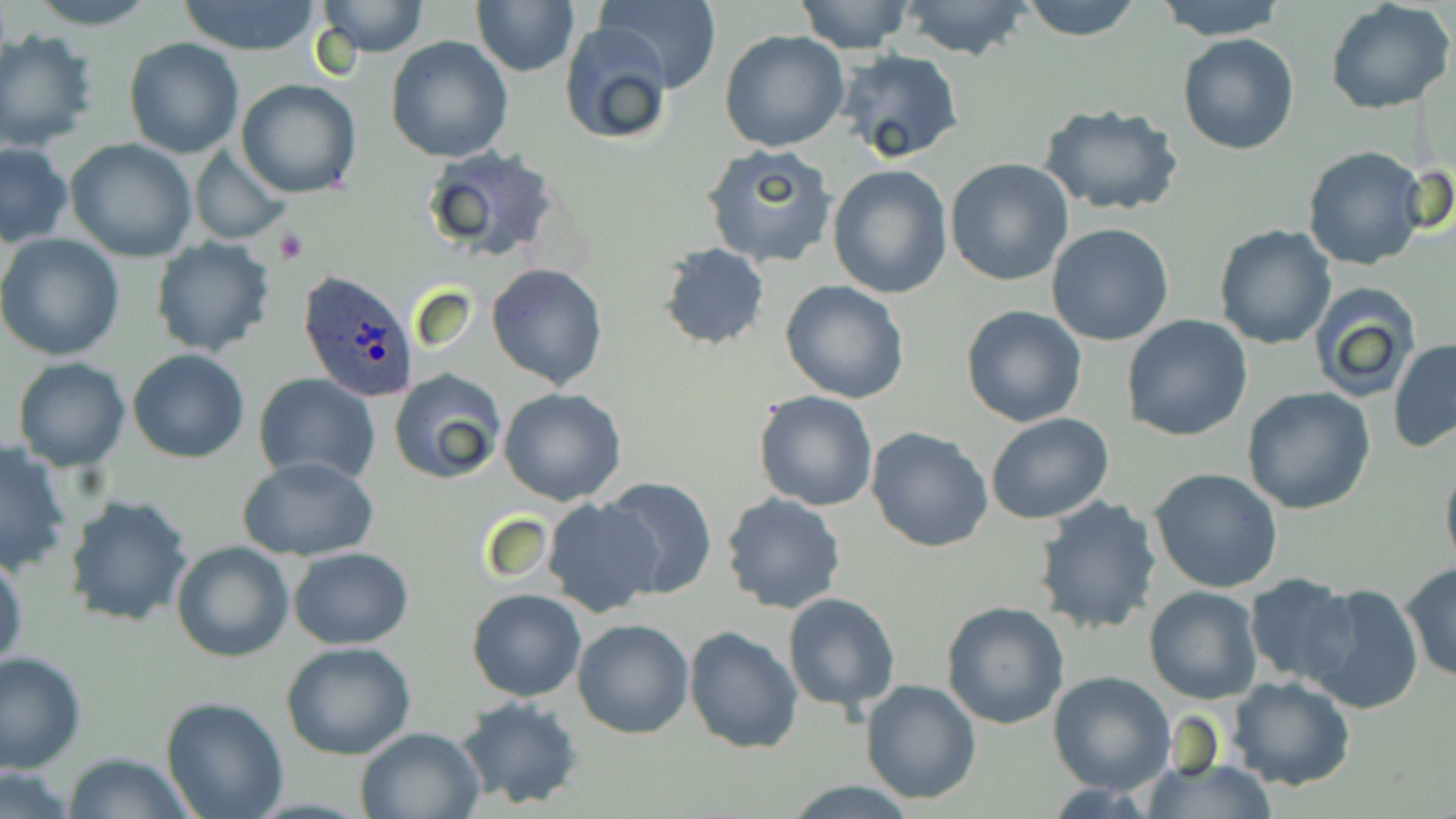

Approximate bounding boxes as [x1, y1, x2, y2] in pixels. Uninfected red blood cell locations: [21, 0, 161, 29], [173, 0, 324, 55], [315, 0, 431, 57], [793, 0, 915, 54], [898, 0, 1034, 62], [1016, 0, 1144, 42], [1152, 0, 1289, 41], [1324, 0, 1454, 115], [472, 1, 579, 76], [596, 1, 722, 93], [556, 23, 675, 147], [1, 28, 101, 152], [720, 29, 850, 152], [1176, 33, 1300, 155], [124, 37, 244, 159], [386, 37, 513, 161], [836, 50, 966, 168], [235, 79, 362, 199], [1037, 103, 1183, 216], [65, 139, 199, 261], [0, 143, 73, 248], [702, 143, 839, 269], [1302, 143, 1431, 271], [422, 145, 564, 259], [188, 146, 290, 244], [944, 157, 1075, 286], [827, 165, 953, 299], [1047, 224, 1176, 347], [1214, 224, 1337, 350], [0, 235, 125, 361], [149, 236, 275, 357], [657, 243, 770, 351], [488, 262, 607, 390], [780, 280, 910, 404], [1308, 282, 1423, 401], [960, 304, 1088, 427], [1121, 314, 1252, 442], [1389, 340, 1456, 452], [128, 350, 250, 462], [13, 356, 131, 471], [388, 370, 507, 484], [254, 374, 380, 484], [499, 387, 626, 505], [1242, 387, 1376, 514], [753, 391, 878, 512], [986, 413, 1115, 526], [866, 425, 995, 552], [0, 441, 73, 575], [1439, 454, 1456, 572], [240, 458, 379, 562], [1149, 468, 1284, 594], [598, 476, 717, 600], [720, 491, 846, 614], [63, 493, 195, 627], [543, 496, 662, 617], [1033, 496, 1162, 636], [171, 540, 293, 662], [288, 546, 413, 649], [0, 548, 26, 674], [1400, 561, 1456, 682], [1244, 575, 1362, 685], [1303, 582, 1427, 716], [1143, 585, 1263, 704], [467, 588, 587, 703], [783, 591, 901, 714], [940, 601, 1070, 729], [571, 618, 693, 739], [684, 627, 802, 754], [280, 641, 416, 760], [1, 652, 86, 772], [1048, 670, 1178, 795], [1227, 675, 1357, 791], [860, 679, 983, 805], [455, 696, 586, 809], [160, 697, 288, 819], [355, 727, 483, 819], [63, 751, 194, 818], [1141, 758, 1280, 817], [0, 764, 80, 818], [779, 780, 923, 816]. Platelet locations: [271, 228, 308, 264]. Plasmodium ovale-infected red blood cell locations: [298, 269, 419, 401]. Slide-level diagnosis: Plasmodium ovale. One field of a larger specimen. May-Grünwald-Giemsa-stained preparation. Captured at 1000x magnification. Light microscopy. Image is 1456×819 pixels. Thin blood film.